Classify this cell by malaria status.
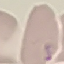
Uninfected.

{
  "image_type": "cell patch, automatically extracted from a larger field of view and resized to 64 × 64 pixels",
  "preparation": "thin blood film",
  "capture": "smartphone through the microscope eyepiece",
  "stain": "Giemsa"
}